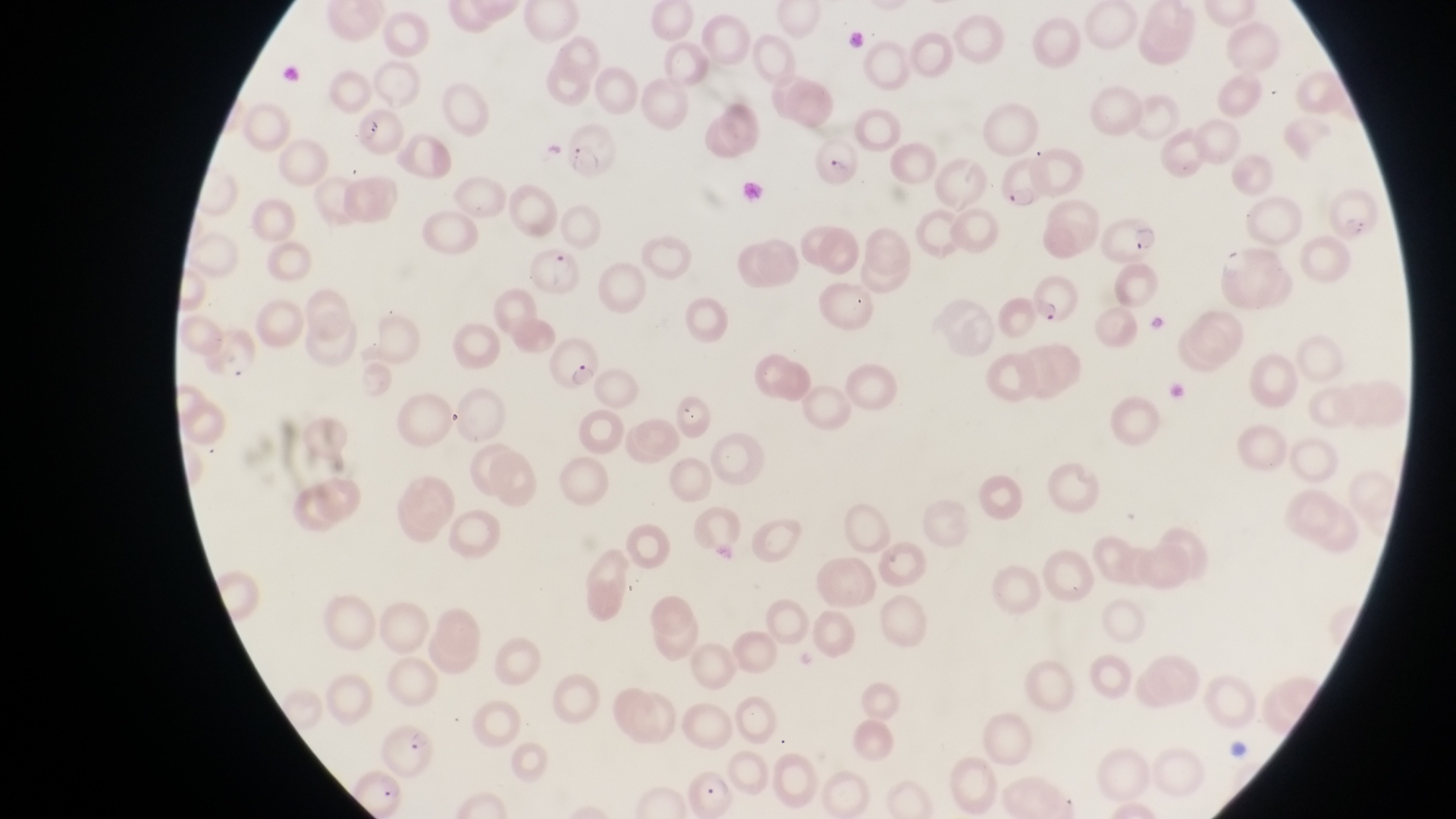

magnification = 1000x
capture = smartphone photograph through the eyepiece of an Olympus CX-23 microscope
country = Uganda
parasitised red blood cell locations = approximate bounding boxes as [left, top, right, bottom] in pixels: [354, 111, 403, 158], [565, 122, 620, 177], [809, 126, 862, 190], [1003, 153, 1049, 214], [1097, 212, 1161, 267], [531, 243, 581, 302], [1215, 246, 1294, 307], [1028, 275, 1083, 330], [541, 334, 601, 390], [383, 723, 430, 773], [689, 767, 742, 817]
preparation = thin blood film
artifact (platelet-like body, stain precipitate, or debris) locations = approximate bounding boxes as [left, top, right, bottom] in pixels: [1329, 185, 1389, 248], [1145, 311, 1169, 345]
field of view = single
image size = 1456×819 pixels